Comment on the morphology of the red blood cells.
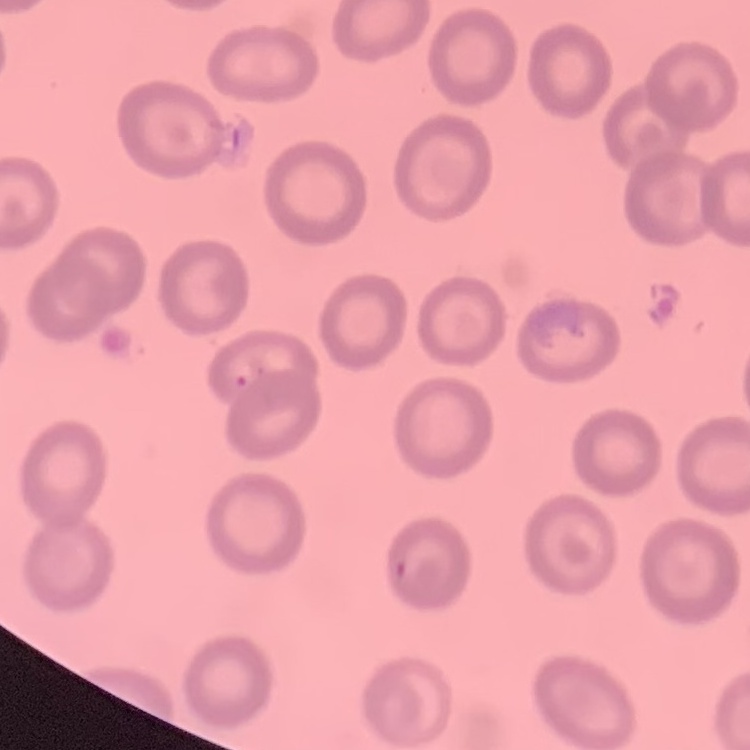
No rouleaux formation.

image type = square crop of a larger photomicrograph
stain = Field's or Giemsa
preparation = thin blood smear